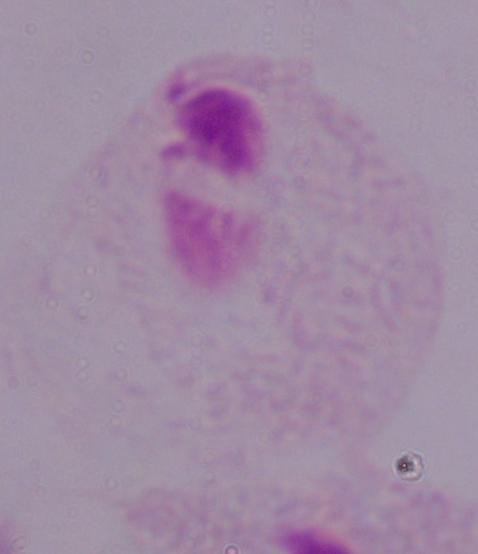 1000x magnification. A trichomonad is shown. Micrograph.